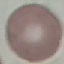

Summary:
  - Malaria status: uninfected
  - Capture: smartphone camera at the microscope eyepiece
  - Stain: Giemsa
  - Preparation: thin smear
  - Image type: cell patch, automatically extracted from a larger field of view and resized to 64 × 64 pixels